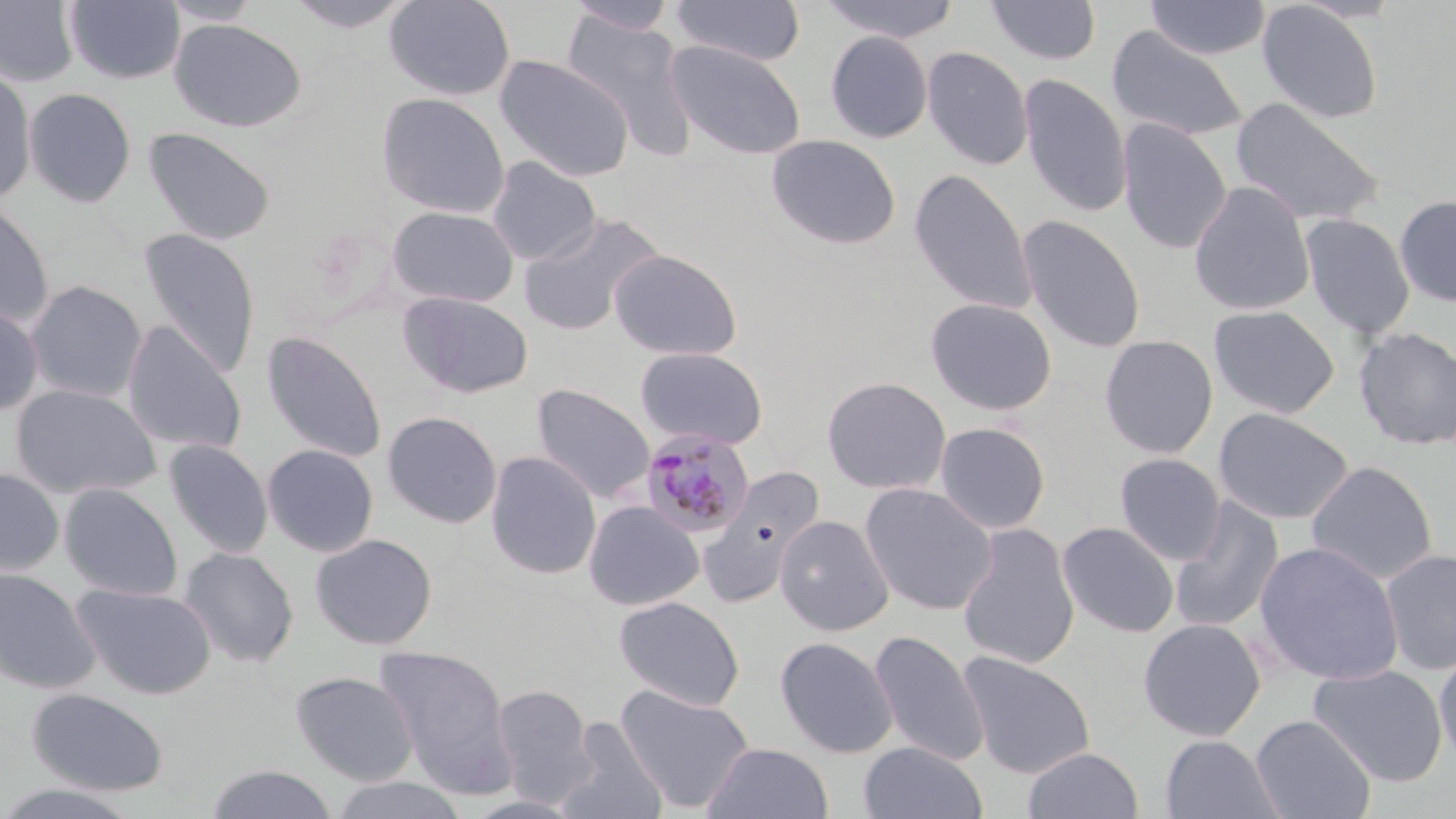 Approximate bounding boxes as [x1, y1, x2, y2] in pixels. Plasmodium malariae-infected red blood cell locations: [639, 428, 754, 538]. Uninfected red blood cell locations: [0, 0, 79, 87], [65, 0, 184, 85], [284, 0, 416, 32], [384, 0, 516, 102], [564, 0, 680, 35], [671, 0, 806, 66], [820, 0, 960, 43], [158, 1, 263, 26], [986, 1, 1101, 65], [1145, 1, 1272, 60], [1257, 2, 1382, 124], [562, 13, 697, 157], [169, 19, 307, 133], [1107, 26, 1248, 143], [824, 31, 933, 145], [664, 40, 806, 160], [921, 46, 1034, 170], [493, 55, 635, 181], [0, 68, 36, 206], [1018, 73, 1132, 218], [23, 88, 136, 207], [375, 93, 510, 218], [1229, 97, 1384, 227], [1116, 118, 1232, 254], [143, 128, 276, 246], [766, 134, 902, 250], [486, 157, 601, 265], [909, 168, 1037, 315], [1189, 182, 1315, 316], [1395, 195, 1456, 306], [0, 201, 54, 329], [386, 206, 519, 308], [518, 212, 664, 336], [1016, 214, 1146, 353], [1300, 214, 1416, 339], [137, 229, 260, 379], [609, 249, 741, 361], [25, 280, 147, 403], [398, 292, 534, 399], [925, 297, 1057, 416], [0, 302, 43, 417], [1208, 305, 1339, 420], [122, 322, 247, 456], [1352, 327, 1456, 451], [262, 331, 387, 463], [1099, 335, 1218, 458], [634, 346, 768, 450], [821, 376, 951, 495], [10, 384, 160, 500], [531, 385, 655, 504], [1213, 408, 1354, 525], [381, 411, 502, 529], [934, 422, 1051, 534], [164, 440, 273, 559], [262, 444, 378, 557], [485, 450, 601, 581], [1114, 453, 1226, 565], [1305, 461, 1438, 585], [697, 465, 827, 607], [0, 468, 64, 576], [59, 482, 183, 602], [859, 483, 998, 615], [1169, 497, 1285, 634], [583, 500, 704, 611], [774, 514, 895, 636], [1057, 521, 1179, 638], [956, 523, 1080, 670], [310, 533, 437, 650], [1254, 541, 1404, 686], [179, 548, 299, 667], [1380, 548, 1456, 675], [0, 567, 100, 693], [71, 583, 216, 700], [614, 596, 745, 711], [1138, 618, 1266, 741], [868, 631, 989, 766], [774, 636, 898, 759], [374, 644, 516, 792], [1433, 648, 1456, 769], [956, 651, 1095, 779], [1308, 664, 1447, 787], [290, 671, 418, 785], [490, 683, 596, 807], [616, 685, 755, 814], [28, 688, 169, 796], [1250, 714, 1376, 819], [555, 716, 666, 819], [1159, 734, 1284, 819], [857, 740, 989, 819], [702, 742, 834, 819], [1021, 747, 1144, 819], [206, 763, 338, 819], [327, 775, 469, 819], [0, 782, 141, 818]. Slide-level diagnosis: Plasmodium malariae. Thin blood smear. Light microscopy. Image is 1456×819 pixels. May-Grünwald-Giemsa-stained preparation. 1000x magnification. Single field of view.